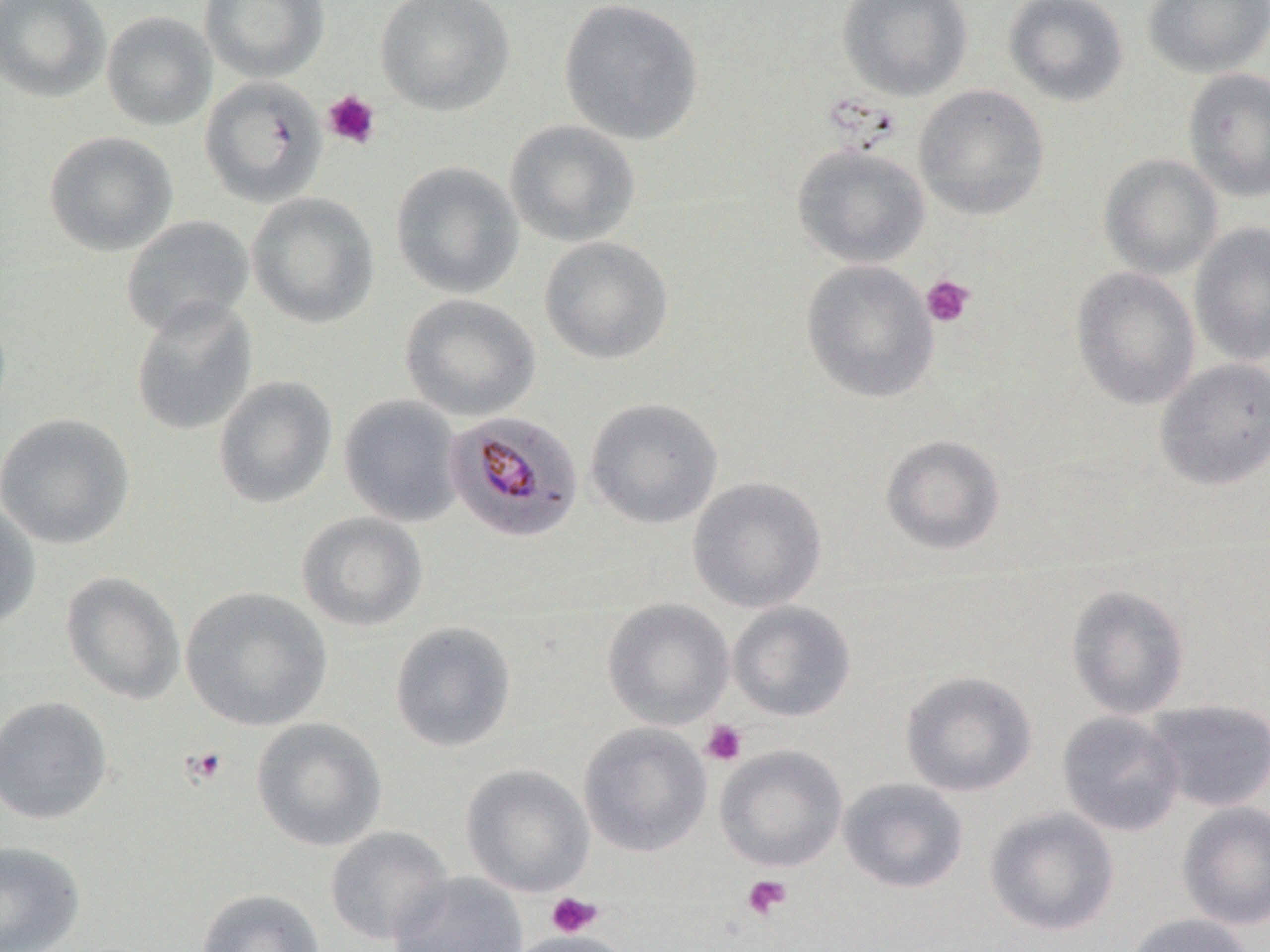

Approximate bounding boxes as (x1, y1, x2, y2) in pixels. Plasmodium malariae-infected red blood cell locations: (445, 408, 584, 542). Uninfected red blood cell locations: (0, 0, 111, 104), (199, 0, 331, 84), (375, 0, 515, 116), (837, 0, 973, 102), (1004, 0, 1129, 107), (1143, 0, 1270, 79), (557, 1, 705, 145), (100, 10, 217, 131), (1182, 67, 1270, 203), (199, 75, 328, 208), (912, 84, 1050, 221), (503, 119, 641, 248), (43, 131, 178, 256), (791, 143, 931, 269), (1099, 153, 1224, 280), (390, 160, 524, 299), (246, 191, 380, 328), (120, 214, 255, 338), (1189, 222, 1270, 367), (539, 236, 674, 365), (800, 259, 940, 404), (1071, 266, 1200, 410), (399, 293, 541, 422), (129, 298, 258, 436), (1154, 357, 1270, 490), (212, 375, 337, 509), (339, 395, 464, 527), (585, 397, 724, 530), (0, 412, 135, 550), (880, 433, 1006, 556), (687, 476, 827, 614), (0, 501, 42, 629), (295, 510, 428, 632), (59, 570, 186, 705), (1065, 584, 1190, 720), (179, 585, 333, 732), (601, 597, 735, 731), (727, 600, 857, 723), (389, 620, 517, 753), (900, 670, 1038, 797), (0, 694, 114, 826), (1145, 699, 1269, 812), (1056, 710, 1186, 837), (251, 716, 387, 852), (578, 721, 713, 858), (714, 743, 848, 873), (460, 763, 595, 897), (837, 777, 969, 894), (1177, 801, 1270, 930), (984, 806, 1120, 937), (324, 826, 454, 946), (0, 839, 86, 952), (386, 871, 529, 952), (196, 888, 326, 952), (1124, 912, 1254, 952), (506, 930, 634, 952). Platelet locations: (321, 90, 382, 150), (920, 275, 975, 328), (700, 720, 747, 766), (180, 745, 230, 787), (741, 874, 791, 921), (546, 892, 602, 938). Slide-level diagnosis: Plasmodium malariae. Thin blood smear. Optical microscopy. May-Grünwald-Giemsa-stained preparation. 1000x magnification. Single field of view. Image is 1270×952 pixels.